Outline each blood parasite and name the species.
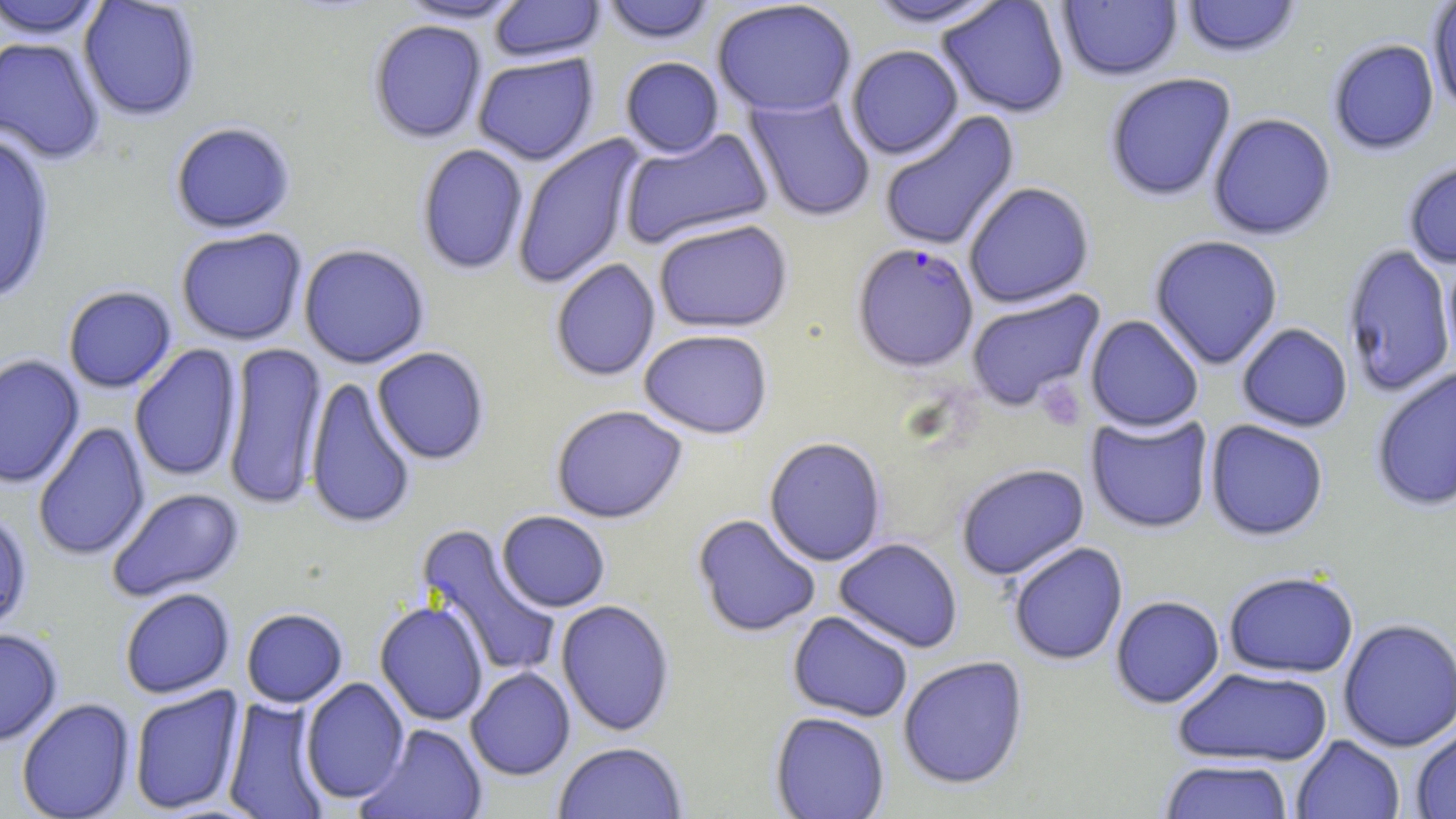
Approximate bounding boxes as (x1, y1, x2, y2) in pixels.
Plasmodium falciparum-infected red blood cells: (852, 242, 979, 373).
No Plasmodium ovale, Plasmodium malariae, Plasmodium vivax, Babesia divergens, or Trypanosoma brucei observed.

Uninfected red blood cell locations: (395, 0, 528, 25), (488, 0, 604, 64), (600, 0, 718, 47), (861, 0, 1010, 31), (936, 0, 1070, 119), (1179, 0, 1303, 59), (0, 1, 109, 40), (78, 1, 202, 122), (711, 1, 858, 117), (1057, 1, 1183, 82), (1427, 1, 1456, 114), (368, 20, 487, 143), (0, 37, 106, 165), (1327, 39, 1439, 156), (845, 46, 964, 161), (473, 53, 599, 166), (619, 57, 725, 158), (1105, 73, 1237, 203), (745, 94, 876, 223), (879, 110, 1020, 252), (1207, 113, 1337, 240), (170, 122, 296, 234), (619, 127, 774, 249), (0, 131, 56, 304), (511, 134, 643, 290), (416, 143, 529, 276), (1402, 158, 1456, 270), (963, 182, 1095, 309), (653, 219, 794, 334), (175, 227, 308, 345), (1148, 235, 1284, 370), (1341, 243, 1456, 398), (298, 244, 430, 369), (1442, 250, 1456, 375), (550, 258, 660, 382), (62, 286, 177, 393), (965, 289, 1106, 412), (1084, 315, 1204, 433), (1236, 323, 1353, 433), (638, 329, 774, 439), (221, 342, 328, 511), (129, 344, 243, 483), (372, 347, 490, 466), (0, 354, 85, 489), (1370, 366, 1456, 513), (304, 376, 417, 530), (551, 405, 688, 523), (1085, 412, 1214, 534), (1204, 419, 1329, 541), (32, 421, 150, 562), (764, 437, 887, 567), (954, 463, 1090, 581), (106, 487, 246, 602), (0, 511, 33, 637), (496, 511, 610, 613), (692, 514, 821, 638), (416, 524, 562, 680), (833, 538, 963, 654), (1008, 542, 1128, 666), (1222, 570, 1359, 678), (119, 587, 235, 699), (1110, 595, 1225, 709), (555, 599, 675, 737), (374, 600, 489, 726), (241, 608, 348, 708), (787, 611, 914, 723), (1338, 619, 1456, 752), (0, 628, 63, 746), (897, 656, 1029, 790), (465, 667, 576, 780), (1172, 667, 1334, 767), (299, 677, 410, 804), (129, 685, 244, 815), (16, 698, 135, 819), (221, 698, 330, 819), (770, 711, 891, 819), (357, 723, 488, 819), (1411, 724, 1456, 818), (1290, 734, 1405, 819), (553, 741, 688, 818), (1159, 759, 1294, 819). Platelet locations: (1035, 379, 1087, 432). Slide-level diagnosis: Plasmodium falciparum. May-Grünwald-Giemsa-stained preparation. Light microscopy. Captured at 1000x magnification. One field of a larger specimen. Thin blood smear. Image is 1456×819 pixels.